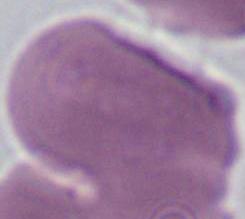

Summary:
  - Magnification: 1000x
  - Modality: photomicrograph
  - Identification: erythrocyte